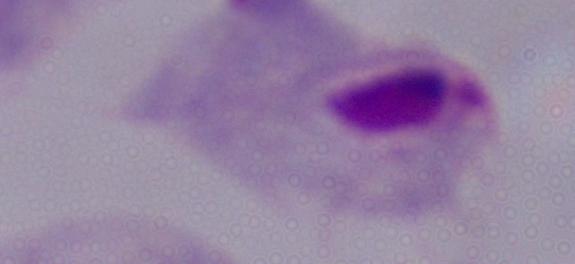
Summary:
  - Identification: trichomonad
  - Magnification: 1000x
  - Modality: photomicrograph